Classify this cell by malaria status.
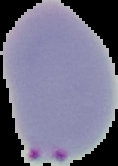

Parasitized.

The area outside the segmented cell region is set to black. Image is 118×166 pixels. From a thin blood smear.